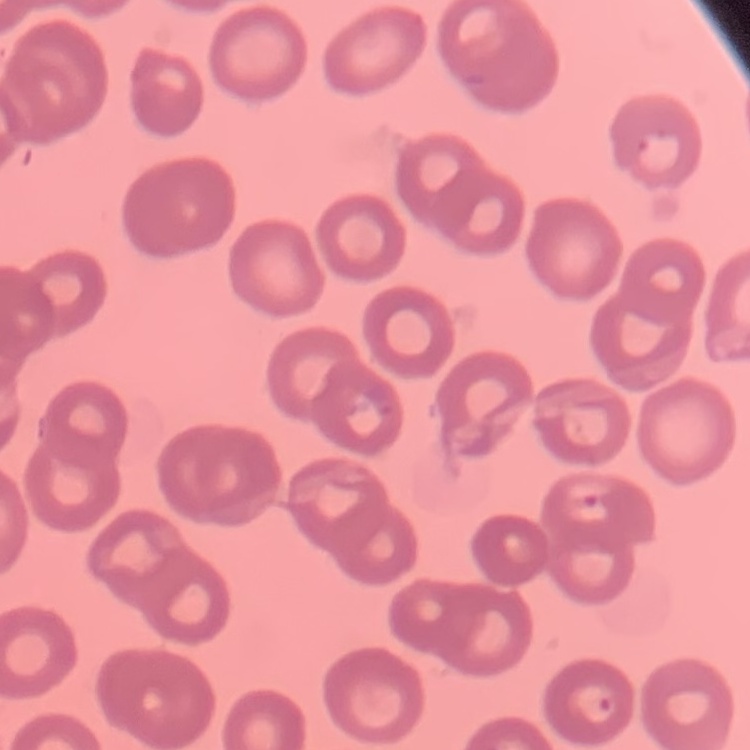

{
  "red_blood_cell_morphology": "no rouleaux formation",
  "preparation": "thin peripheral smear",
  "stain": "Field's or Giemsa",
  "image_type": "square crop of a larger photomicrograph"
}